State which parasite is depicted.
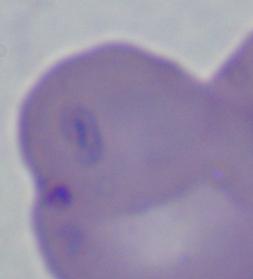

This is Babesia.

Summary:
  - Magnification: 1000x
  - Modality: micrograph